Find the cells and give the type of each one.
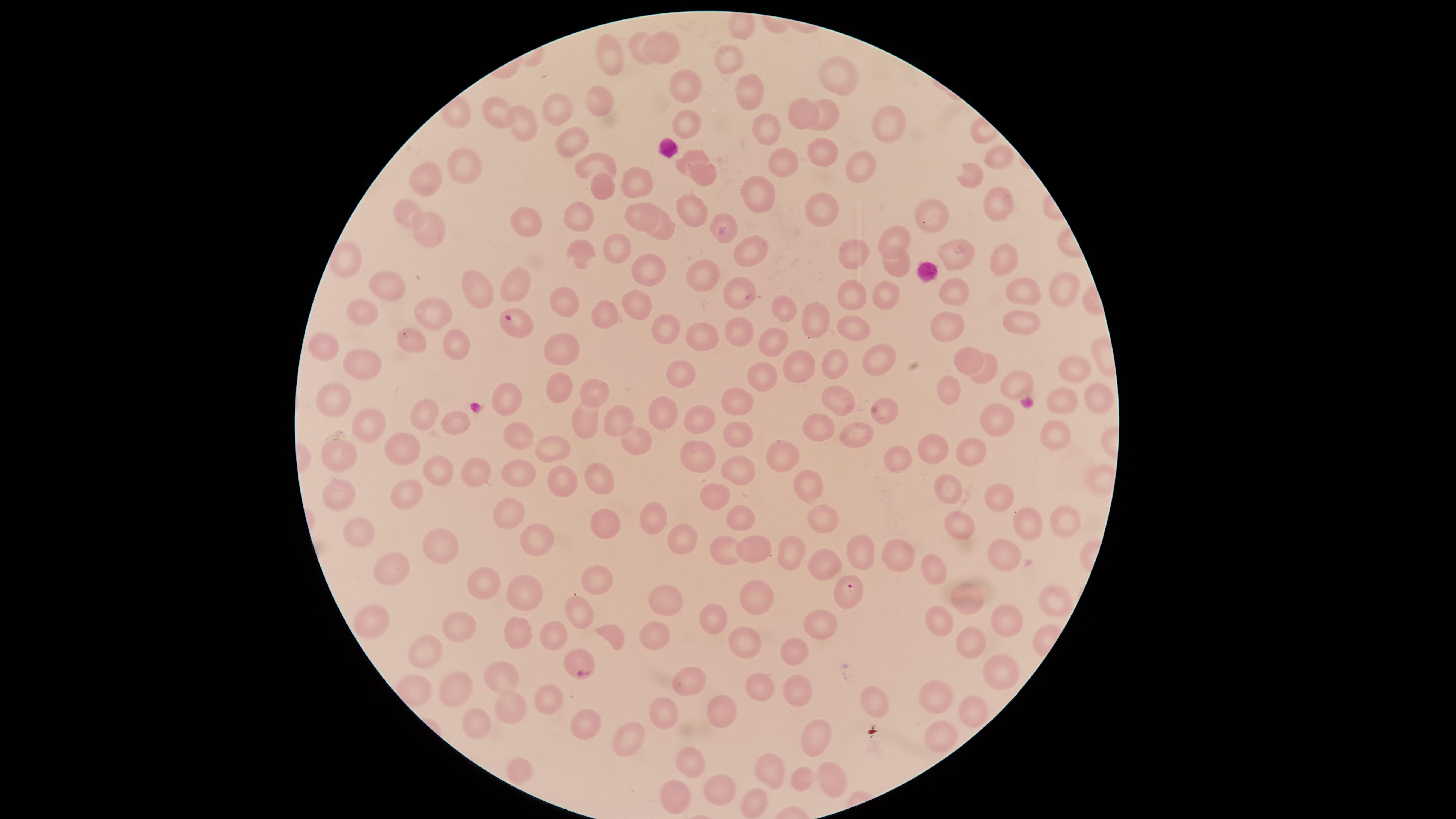
Approximate marker points as (x, y) in pixels.
Parasitized red blood cells: (514, 323), (849, 592), (579, 663).
Uninfected red blood cells: (743, 28), (667, 42), (636, 43), (612, 56), (730, 60), (837, 76), (685, 90), (749, 91), (595, 101), (562, 106), (501, 107), (799, 107), (685, 120), (829, 120), (521, 124), (886, 126), (763, 133), (567, 143), (694, 153), (820, 154), (997, 155), (781, 160), (595, 163), (464, 165), (854, 168), (703, 175), (430, 176), (970, 179), (639, 189), (596, 191), (757, 200), (997, 202), (822, 208), (638, 210), (406, 212), (691, 212), (932, 218), (528, 223), (719, 223), (427, 231), (666, 232), (894, 238), (622, 246), (745, 250), (851, 252), (953, 252), (999, 261), (894, 265), (647, 268), (704, 273), (510, 282), (1063, 287), (738, 289), (954, 289), (396, 291), (1024, 291), (883, 292), (476, 297), (852, 297), (634, 302), (558, 303), (366, 306), (780, 308), (435, 313), (607, 315), (944, 322), (1024, 322), (817, 325), (665, 328), (856, 329), (738, 331), (702, 336), (409, 341), (457, 342), (772, 344), (330, 347), (561, 351), (970, 356), (876, 361), (362, 362), (835, 364), (805, 365), (683, 372), (987, 372), (1075, 372), (761, 375), (1019, 377), (562, 385), (336, 394), (945, 395), (1097, 396), (841, 397), (508, 398), (594, 399), (738, 401), (1058, 401), (883, 408), (663, 411), (425, 412), (378, 417), (579, 419), (616, 419), (450, 420), (697, 420), (997, 420), (816, 427), (369, 428), (1054, 430), (518, 431), (736, 431), (855, 434), (631, 437), (403, 449), (555, 449), (939, 450), (974, 451), (334, 453), (780, 453), (898, 455), (703, 456), (738, 469), (437, 472), (522, 473), (476, 474), (600, 479), (562, 480), (813, 487), (948, 491), (404, 492), (712, 494), (342, 497), (1002, 498), (509, 511), (817, 515), (655, 516), (741, 516), (600, 523), (1027, 523), (1063, 524), (956, 530), (359, 536), (542, 538), (676, 542), (435, 549), (723, 552), (753, 552), (792, 552), (860, 552), (1003, 552), (896, 558), (819, 562), (933, 565), (389, 568), (484, 584), (596, 584), (756, 592), (970, 597), (522, 599), (668, 599), (1044, 604), (581, 611), (1004, 612), (937, 618), (713, 619), (364, 621), (460, 626), (817, 626), (517, 628), (654, 631), (552, 632), (613, 634), (745, 640), (970, 651), (425, 654), (792, 654), (1001, 667), (692, 677), (503, 680), (796, 686), (464, 688), (756, 692), (936, 694), (543, 699), (876, 701), (510, 707), (665, 709), (977, 709), (719, 712), (479, 722), (581, 723), (939, 729), (627, 738), (819, 739), (690, 765), (773, 769), (515, 770), (801, 778), (831, 778), (720, 788), (673, 795), (749, 803).
No white blood cells identified.

The visible region is circular. Thin blood smear. Smartphone photograph through the microscope eyepiece. Single field of view. Giemsa stain. Species: Plasmodium falciparum. Image is 1456×819 pixels.